Describe the morphology of the red blood cells.
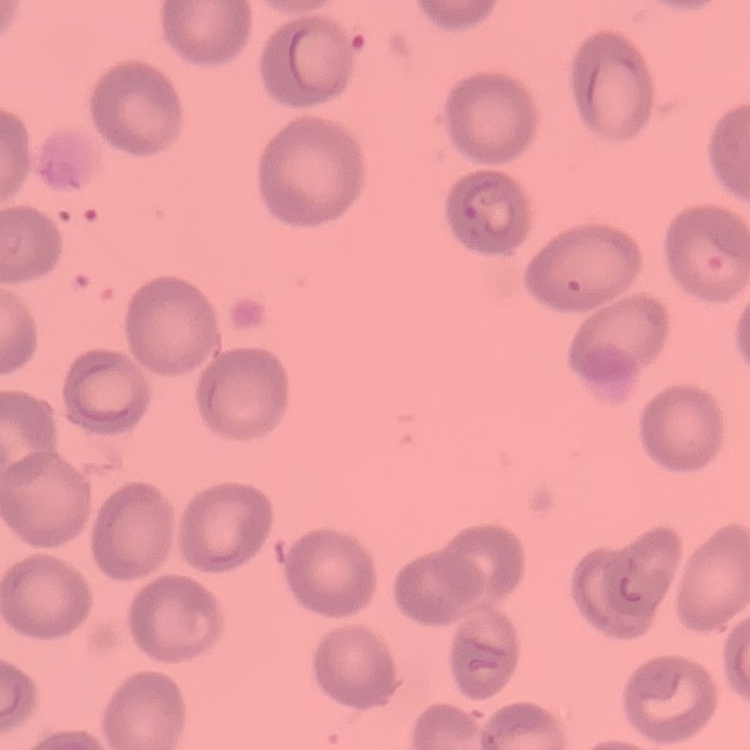

No rouleaux formation.

Field's or Giemsa stain. Thin blood film. Square crop of a larger photomicrograph.